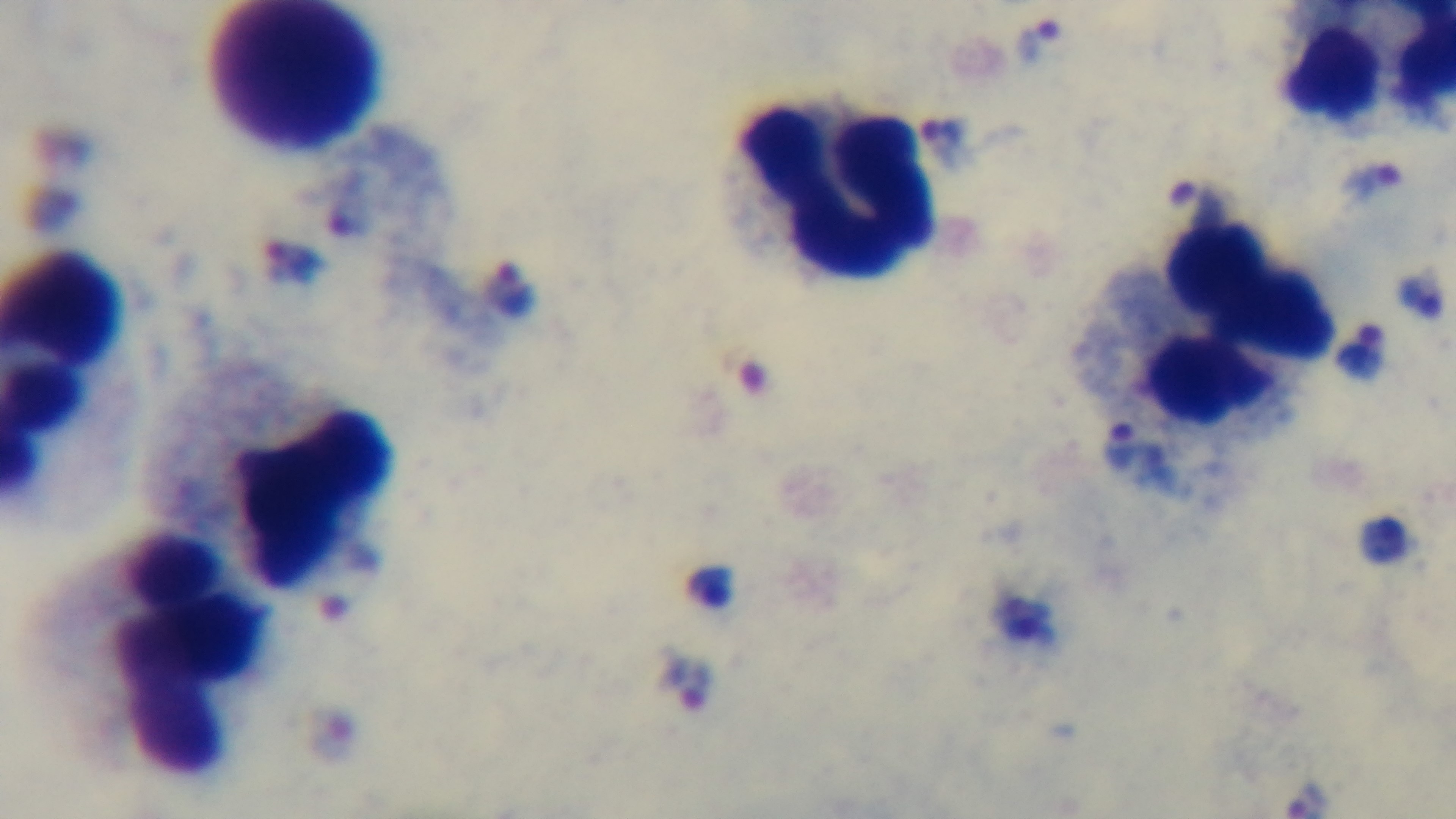
Summary:
  - Objective: 100x oil immersion
  - Field of view: single
  - Malaria status: infected
  - Stain: Giemsa
  - Modality: light microscopy
  - Capture: mounted 4K digital camera
  - Preparation: thick